Classify this cell by malaria status.
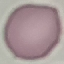

Uninfected.

Giemsa-stained preparation. Thin smear of blood. Acquired by smartphone through the microscope eyepiece. Cell patch, automatically extracted from a larger field of view and resized to 64 × 64 pixels.